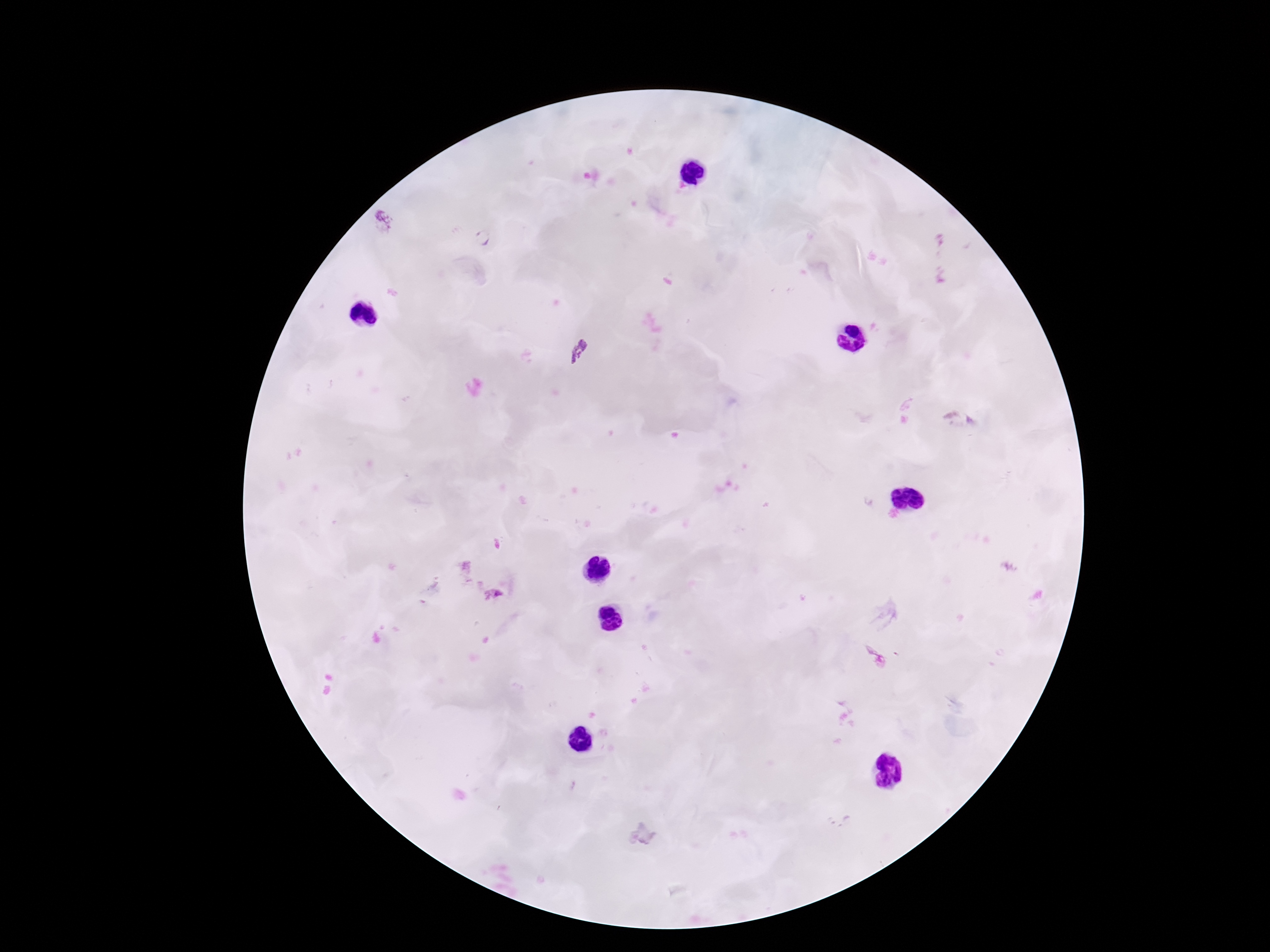
Approximate object centers, in pixels from the top-left corner.
Summary:
  - Plasmodium parasite locations: (x=483, y=238), (x=579, y=351)
  - Stain: Giemsa
  - Magnification: 100x
  - Patient malaria status: infected
  - Image size: 1270×952 pixels
  - Capture: smartphone camera through the microscope eyepiece
  - Field of view: one from this slide
  - Preparation: thick blood smear